Report the malaria status of this cell.
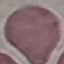

Uninfected.

capture = smartphone through the microscope eyepiece
preparation = thin blood film
stain = Giemsa
image type = cell patch, automatically extracted from a larger field of view and resized to 64 × 64 pixels